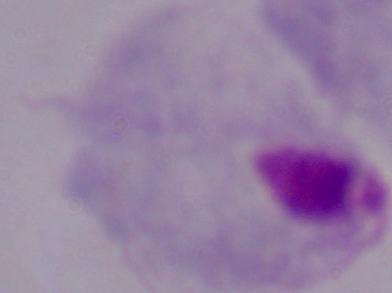
Summary:
  - Identification: trichomonad
  - Modality: photomicrograph
  - Magnification: 1000x